Assess the morphology of the erythrocytes.
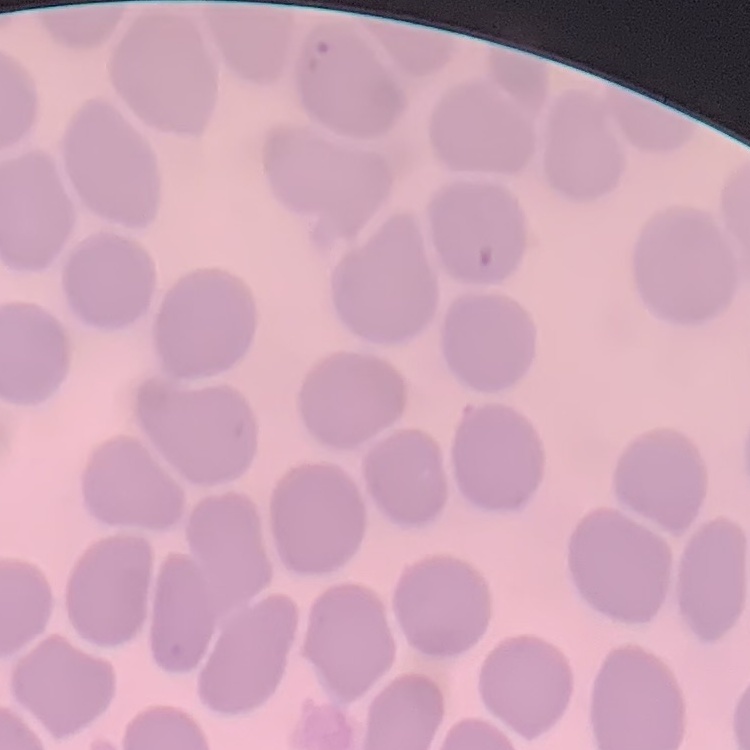
They show no rouleaux formation.

preparation = thin blood smear
image type = square crop of a larger photomicrograph
stain = Field's or Giemsa